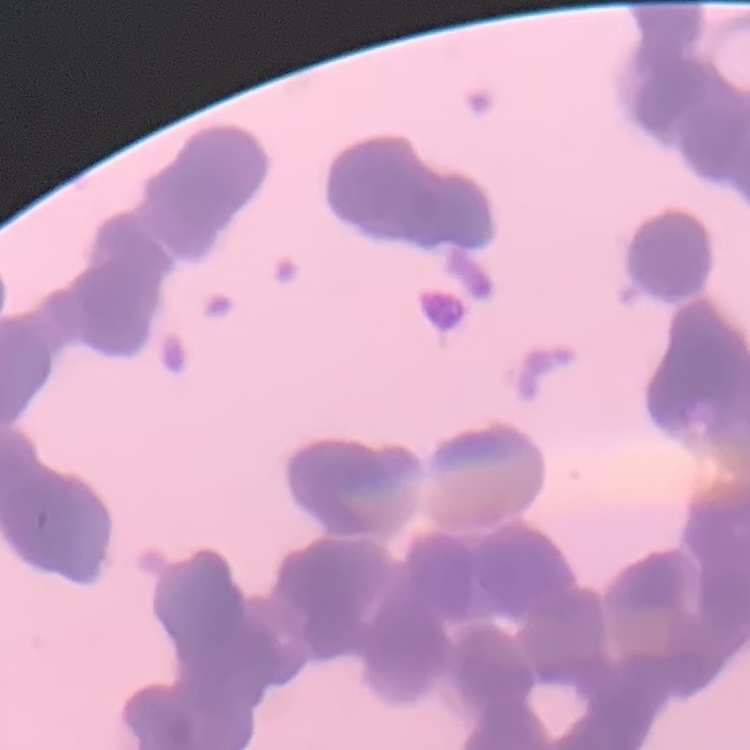
{
  "red_blood_cell_morphology": "rouleaux formation",
  "preparation": "thin blood smear",
  "stain": "Field's or Giemsa",
  "image_type": "square crop of a larger photomicrograph"
}